Locate platelets.
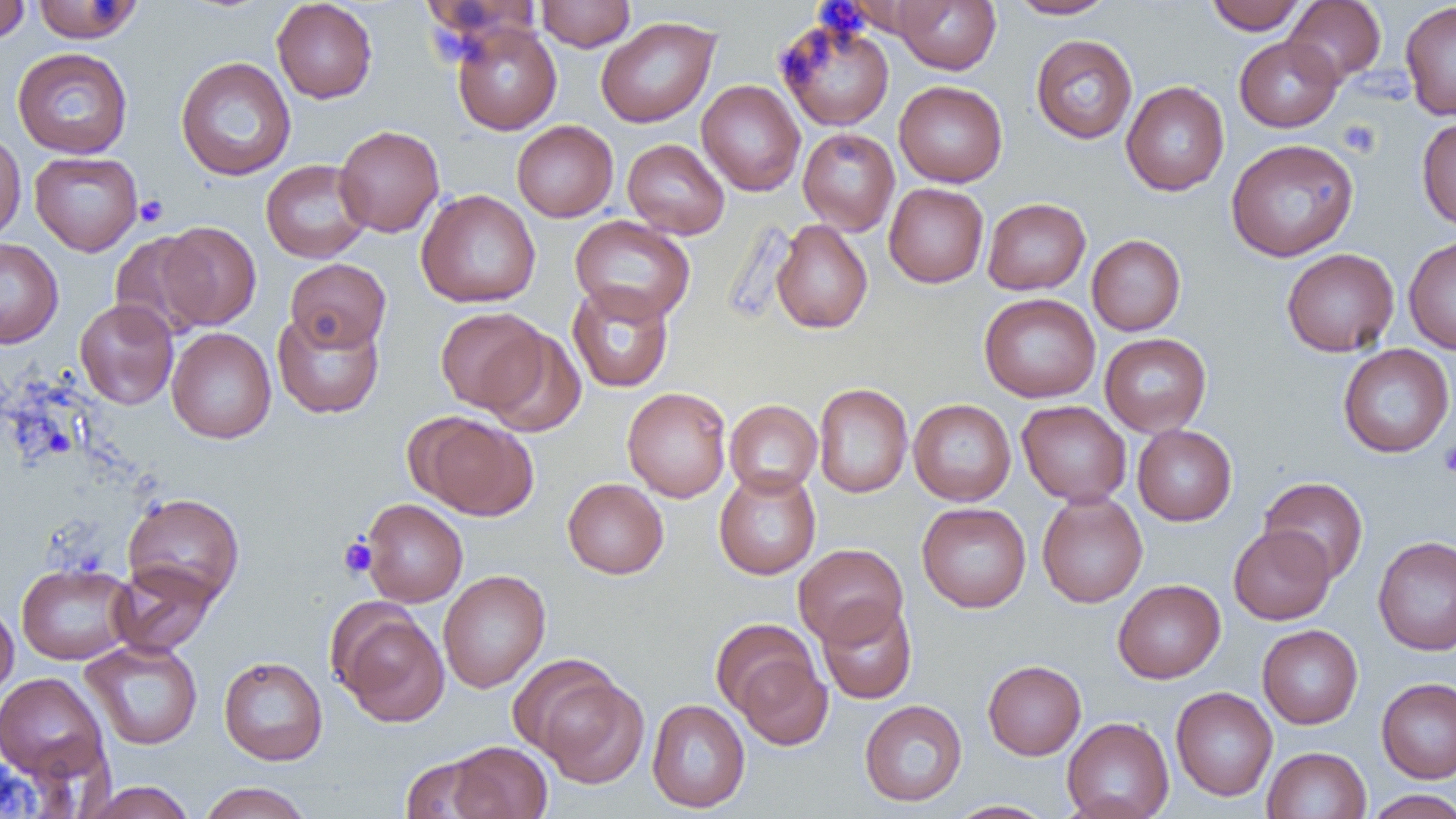

Approximate bounding boxes as [x1, y1, x2, y2] in pixels.
Platelets: [1337, 119, 1381, 158], [135, 195, 169, 227], [1438, 441, 1456, 478], [338, 536, 377, 578].

Uninfected red blood cell locations: [0, 0, 31, 44], [32, 0, 144, 43], [271, 0, 377, 103], [536, 0, 636, 51], [891, 0, 1001, 74], [1007, 0, 1117, 19], [1205, 0, 1308, 34], [1284, 1, 1386, 86], [1400, 1, 1456, 121], [596, 16, 720, 128], [775, 17, 895, 131], [450, 22, 562, 135], [1031, 34, 1138, 144], [1234, 35, 1343, 132], [12, 47, 133, 159], [175, 56, 296, 181], [696, 80, 806, 196], [894, 80, 1008, 187], [1121, 81, 1229, 196], [1416, 116, 1456, 231], [511, 120, 618, 222], [334, 125, 444, 237], [798, 128, 900, 235], [511, 129, 729, 227], [0, 132, 26, 243], [622, 138, 730, 239], [1226, 138, 1359, 262], [30, 151, 143, 256], [261, 159, 372, 263], [884, 182, 988, 288], [415, 189, 541, 308], [982, 197, 1090, 295], [569, 215, 696, 324], [771, 220, 872, 334], [157, 221, 261, 331], [109, 231, 214, 340], [1087, 234, 1186, 335], [1403, 235, 1456, 354], [0, 238, 63, 348], [1281, 248, 1399, 357], [285, 258, 391, 352], [567, 282, 674, 393], [979, 293, 1101, 403], [75, 299, 178, 410], [435, 307, 548, 414], [272, 310, 384, 419], [167, 327, 276, 443], [479, 327, 586, 437], [1099, 332, 1212, 436], [1337, 344, 1455, 458], [813, 383, 913, 498], [622, 387, 732, 502], [725, 399, 822, 497], [908, 399, 1016, 505], [1017, 400, 1132, 507], [411, 412, 537, 520], [1133, 424, 1237, 526], [713, 469, 821, 580], [1259, 477, 1369, 583], [562, 478, 668, 579], [123, 492, 244, 607], [1036, 492, 1148, 607], [361, 498, 468, 607], [917, 502, 1031, 613], [1229, 525, 1335, 624], [1373, 535, 1456, 655], [793, 543, 908, 647], [16, 562, 137, 665], [109, 562, 218, 657], [438, 570, 551, 693], [1113, 579, 1225, 683], [817, 598, 917, 704], [0, 600, 18, 702], [331, 604, 449, 727], [710, 618, 821, 719], [1257, 624, 1363, 729], [80, 639, 203, 749], [732, 650, 833, 751], [218, 656, 328, 765], [983, 660, 1086, 759], [534, 671, 649, 788], [0, 672, 108, 782], [1377, 677, 1456, 784], [1170, 687, 1278, 801], [646, 698, 750, 812], [859, 699, 967, 806], [1062, 717, 1174, 819], [446, 741, 552, 819], [1262, 746, 1371, 819], [400, 754, 497, 818], [79, 781, 197, 818], [198, 782, 314, 819], [1364, 789, 1456, 818], [945, 800, 1058, 818]. Slide-level diagnosis: negative for blood parasites. Image is 1456×819 pixels. Optical microscopy. Thin blood film. One field of a larger specimen. 1000x magnification.